State which parasite is depicted.
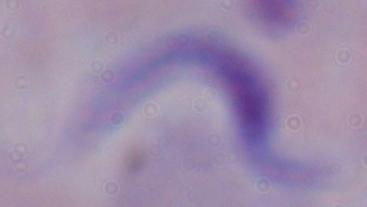

A trypanosome.

Micrograph. Captured at 1000x magnification.